Report the malaria status of this cell.
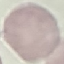

Uninfected.

{
  "stain": "Giemsa",
  "capture": "smartphone through the microscope eyepiece",
  "image_type": "automatically extracted cell patch, resized to 64 × 64 pixels",
  "preparation": "thin blood film"
}